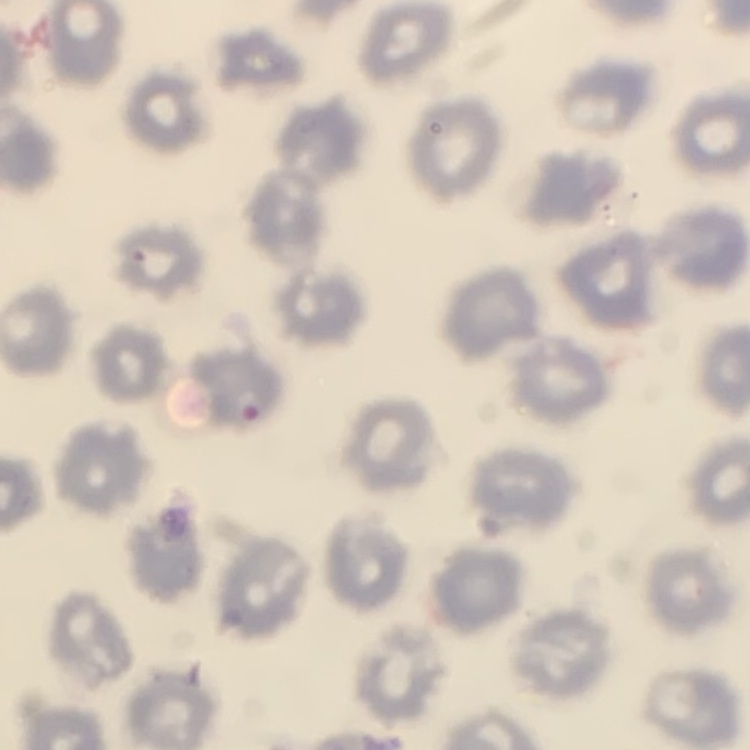

Summary:
  - Erythrocyte morphology: no rouleaux formation
  - Image type: one tile cut from a larger photomicrograph
  - Stain: Field's or Giemsa
  - Preparation: thin peripheral smear